Report the malaria status of this cell.
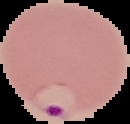
Parasitized.

image size = 130×124 pixels
preparation = thin blood smear
image type = segmented cell region on a black background